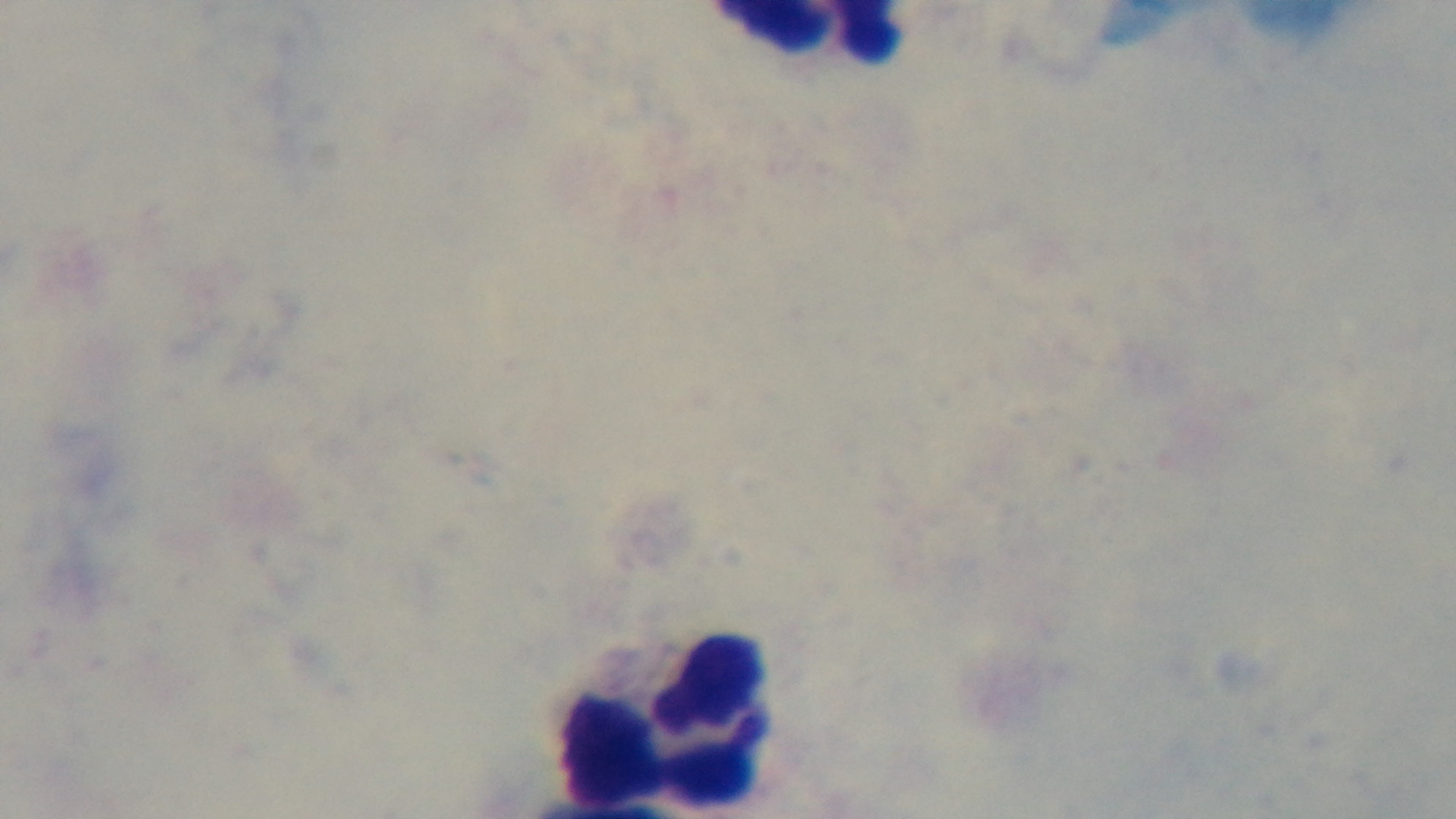
stain = Giemsa
field of view = single
objective = 100x oil immersion
modality = light microscopy
capture = mounted 4K digital camera
preparation = thick blood film
malaria status = uninfected